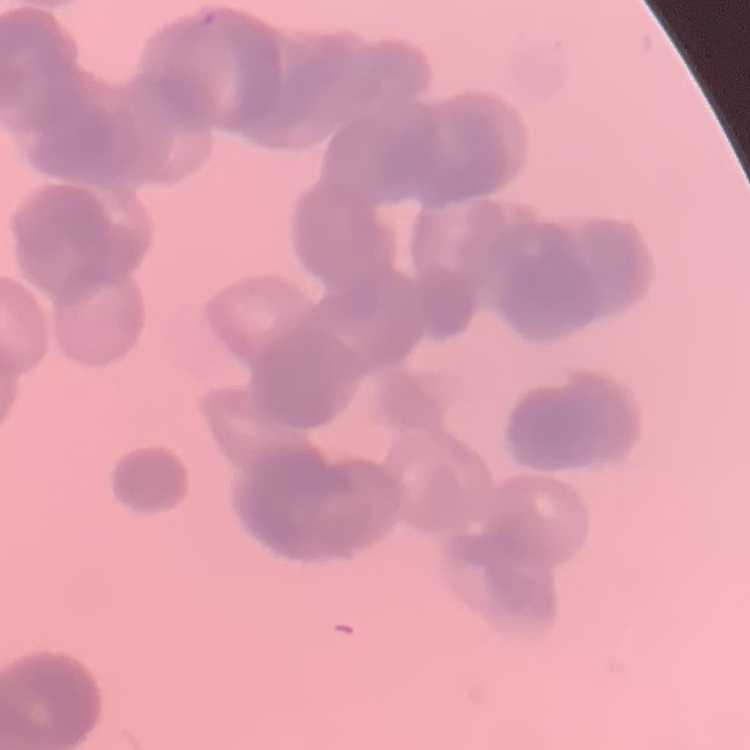
{
  "red_blood_cell_morphology": "rouleaux formation",
  "stain": "Field's or Giemsa",
  "preparation": "thin peripheral smear",
  "image_type": "one tile cut from a larger photomicrograph"
}